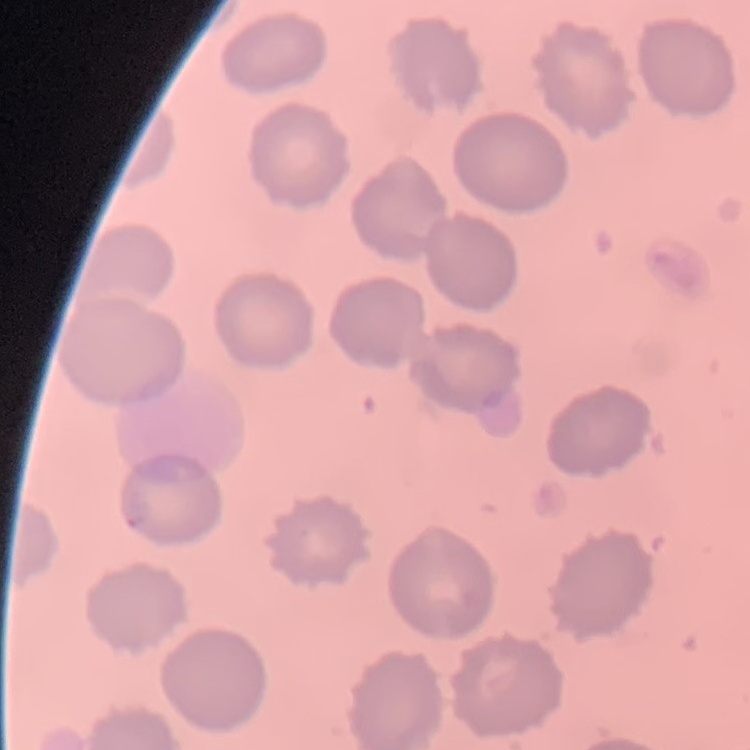
red blood cell morphology = no rouleaux formation
image type = square crop of a larger photomicrograph
stain = Field's or Giemsa
preparation = thin blood film